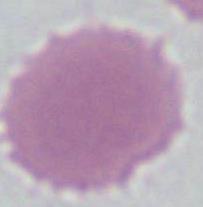

1000x magnification. Micrograph. An erythrocyte is seen.